Assess this cell for malaria.
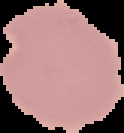

It is uninfected.

Cell region segmented out of the field of view; the surrounding area is masked to black. Image is 124×133 pixels. From a thin blood smear.